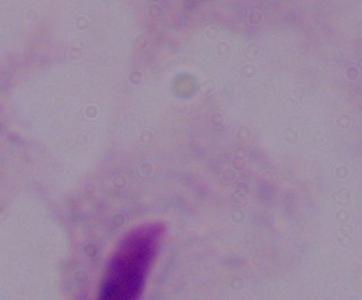
Summary:
  - Identification: trichomonad
  - Modality: micrograph
  - Magnification: 1000x